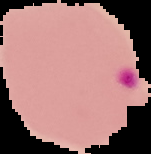
image type = cell region segmented out of the field of view; surrounding area masked to black
preparation = thin blood smear
image size = 151×154 pixels
result = malaria parasites detected